Name the parasite shown.
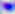
This is Toxoplasma gondii.

Micrograph. 400x magnification.